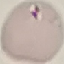 Malaria status: uninfected. Giemsa stain. Thin smear of blood. Automatically extracted cell patch, resized to 64 × 64 pixels. Photographed with a smartphone camera at the microscope eyepiece.